Describe the morphology of the red blood cells.
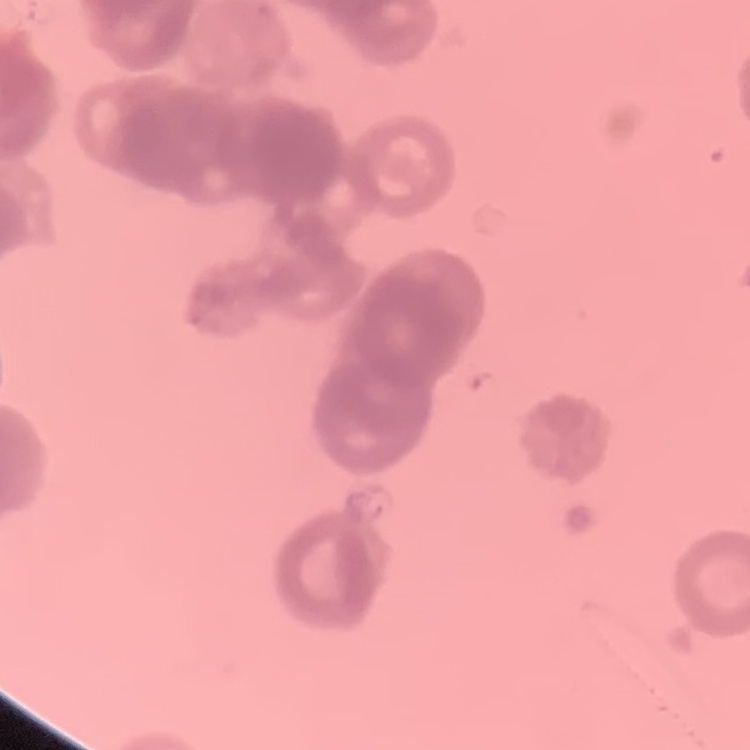

They show rouleaux formation.

image type = one tile cut from a larger photomicrograph
preparation = thin blood smear
stain = Field's or Giemsa